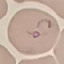

Malaria status: parasitized. Thin blood smear. Acquired by smartphone through the microscope eyepiece. Giemsa-stained preparation. Automatically extracted cell patch, resized to 64 × 64 pixels.